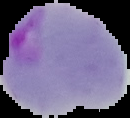
Summary:
  - Image type: segmented cell region on a black background
  - Result: malaria parasites identified
  - Preparation: thin blood smear
  - Image size: 130×118 pixels